Report the malaria status of this cell.
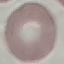

Uninfected.

Giemsa stain. Automatically extracted cell patch, resized to 64 × 64 pixels. Thin smear of blood. Photographed with a smartphone camera at the microscope eyepiece.